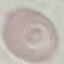 Malaria status: uninfected. Thin blood film. Automatically extracted cell patch, resized to 64 × 64 pixels. Giemsa stain. Acquired by smartphone through the microscope eyepiece.